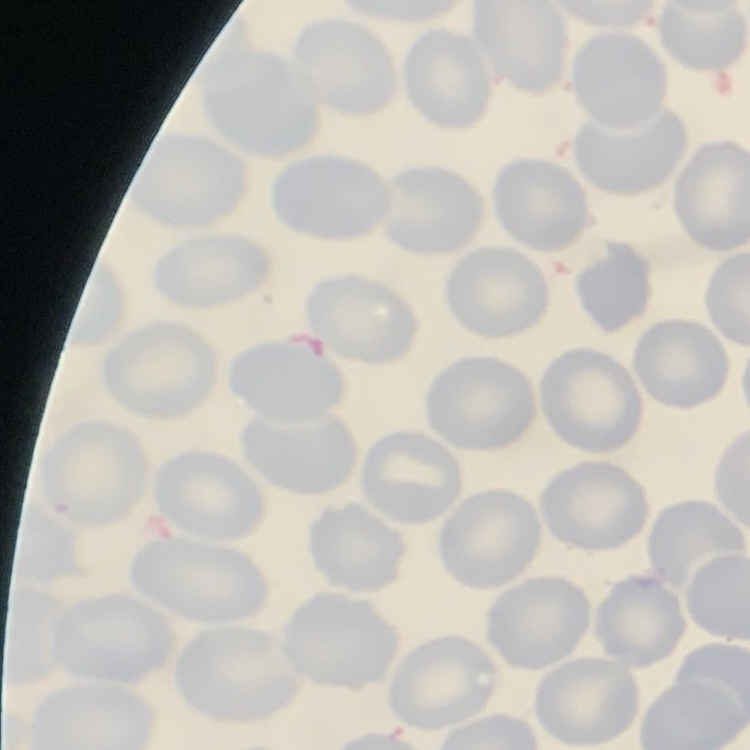

Summary:
  - Erythrocyte morphology: no rouleaux formation
  - Image type: one tile cut from a larger photomicrograph
  - Stain: Field's or Giemsa
  - Preparation: thin blood film